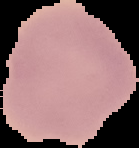

{
  "image_type": "segmented cell region on a black background",
  "preparation": "thin blood smear",
  "image_size": "139×148 pixels",
  "result": "negative for Plasmodium parasites"
}